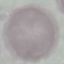
Summary:
  - Malaria status: uninfected
  - Stain: Giemsa
  - Capture: smartphone through the microscope eyepiece
  - Image type: cell patch, automatically extracted from a larger field of view and resized to 64 × 64 pixels
  - Preparation: thin smear